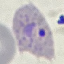
malaria status = parasitized
capture = smartphone camera at the microscope eyepiece
preparation = thin blood smear
image type = cell patch, automatically extracted from a larger field of view and resized to 64 × 64 pixels
stain = Giemsa